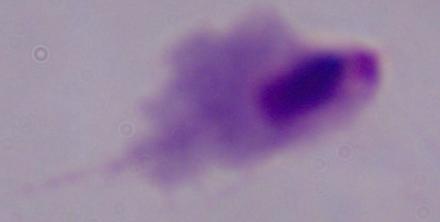
modality = micrograph
magnification = 1000x
identification = trichomonad